Comment on the morphology of the erythrocytes.
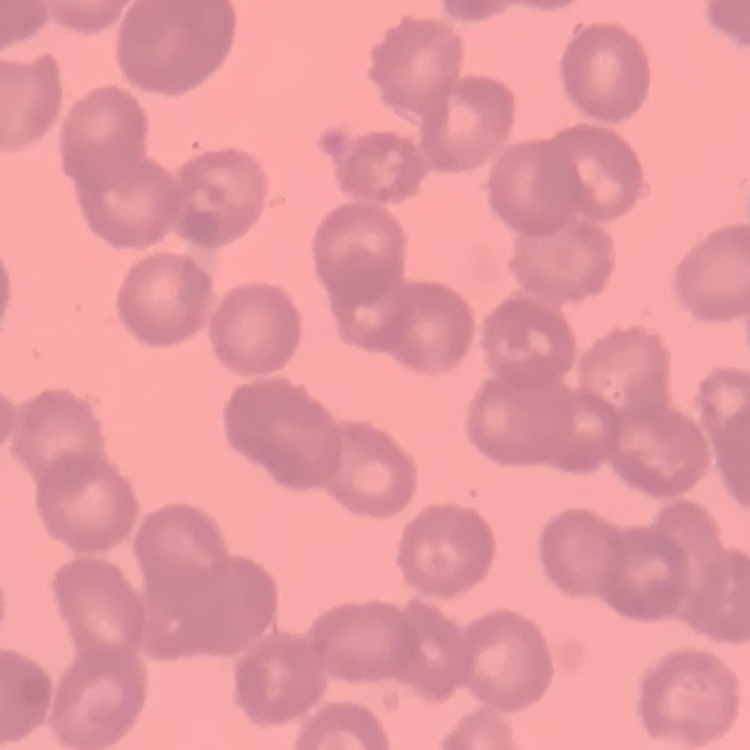

They show rouleaux formation.

preparation: thin blood film
stain: Field's or Giemsa
image_type: square crop of a larger photomicrograph